Give the position of every leukocyte visible.
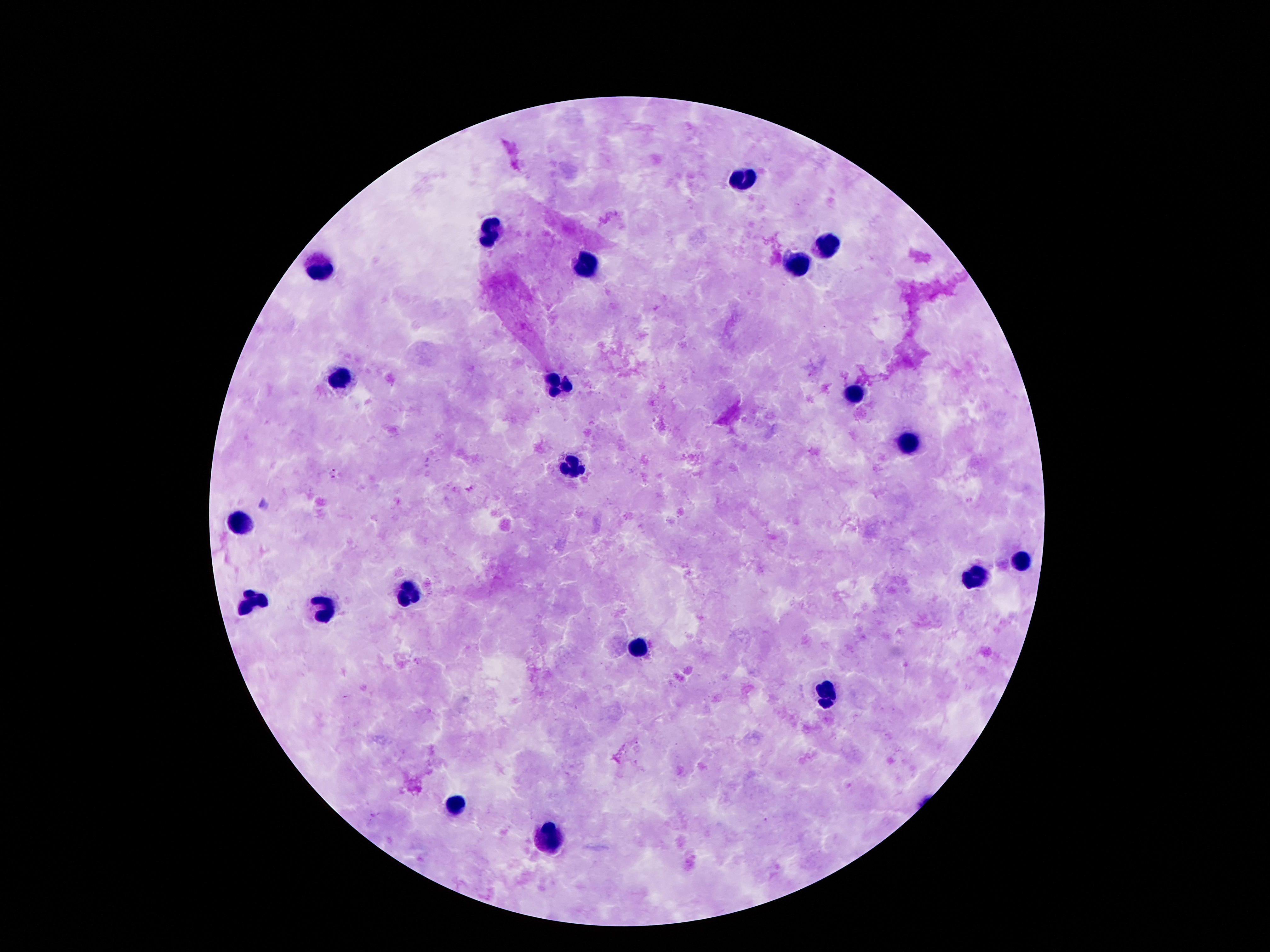

Approximate object centers, in pixels from the top-left corner.
Leukocytes: (x=744, y=179), (x=494, y=231), (x=827, y=241), (x=797, y=263), (x=317, y=268), (x=587, y=268), (x=343, y=378), (x=558, y=392), (x=852, y=394), (x=911, y=449), (x=571, y=469), (x=240, y=520), (x=1022, y=560), (x=976, y=579), (x=408, y=597), (x=255, y=602), (x=323, y=611), (x=642, y=644), (x=825, y=693), (x=456, y=804), (x=556, y=839).

capture = smartphone camera through the microscope eyepiece
stain = Giemsa
preparation = thick peripheral-blood smear
image size = 1270×952 pixels
field of view = single
magnification = 100x
patient malaria status = negative